Classify this cell by malaria status.
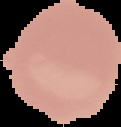

Uninfected.

image_type: segmented cell region on a black background
preparation: thin blood film
image_size: 121×127 pixels